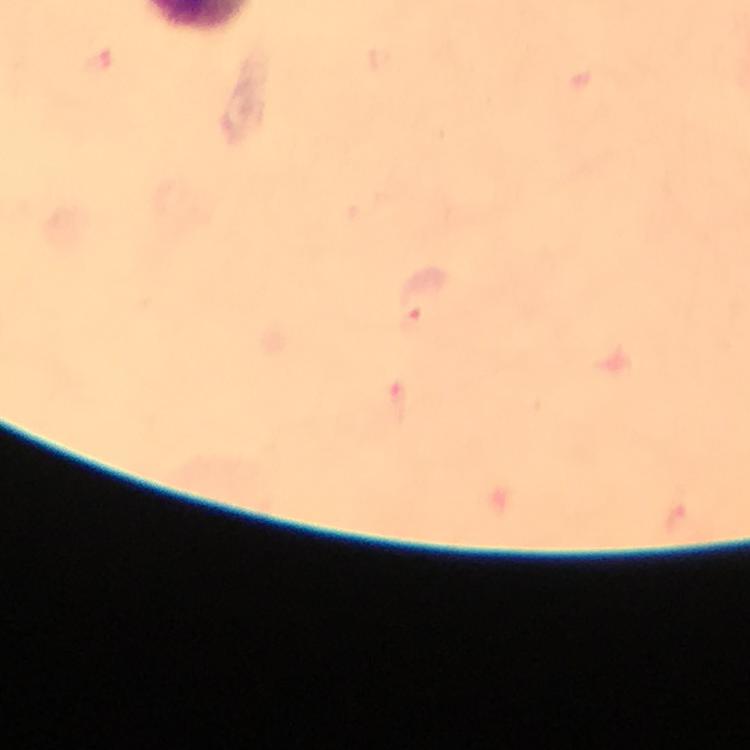

Approximate centers as (x, y) in pixels. Malaria parasite locations: (415, 324). Image is 750×750 pixels. Giemsa-stained preparation. From a malaria diagnostic workup. Photographed with a smartphone mounted on the microscope. Thick blood film. Immersion oil applied. 100x magnification. A crop from one field of view.